Comment on the morphology of the erythrocytes.
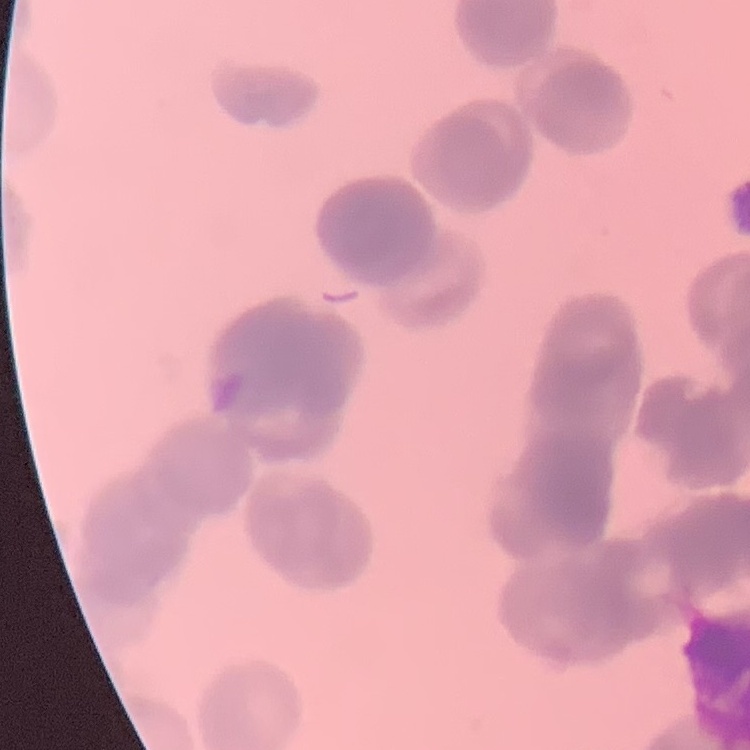

They show rouleaux formation.

Summary:
  - Preparation: thin blood film
  - Stain: Field's or Giemsa
  - Image type: one tile cut from a larger photomicrograph